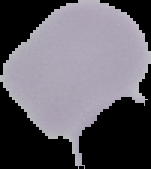 Malaria status: uninfected. From a thin blood smear. Image is 151×169 pixels. Segmented cell region on a black background.